Find each parasitized red blood cell.
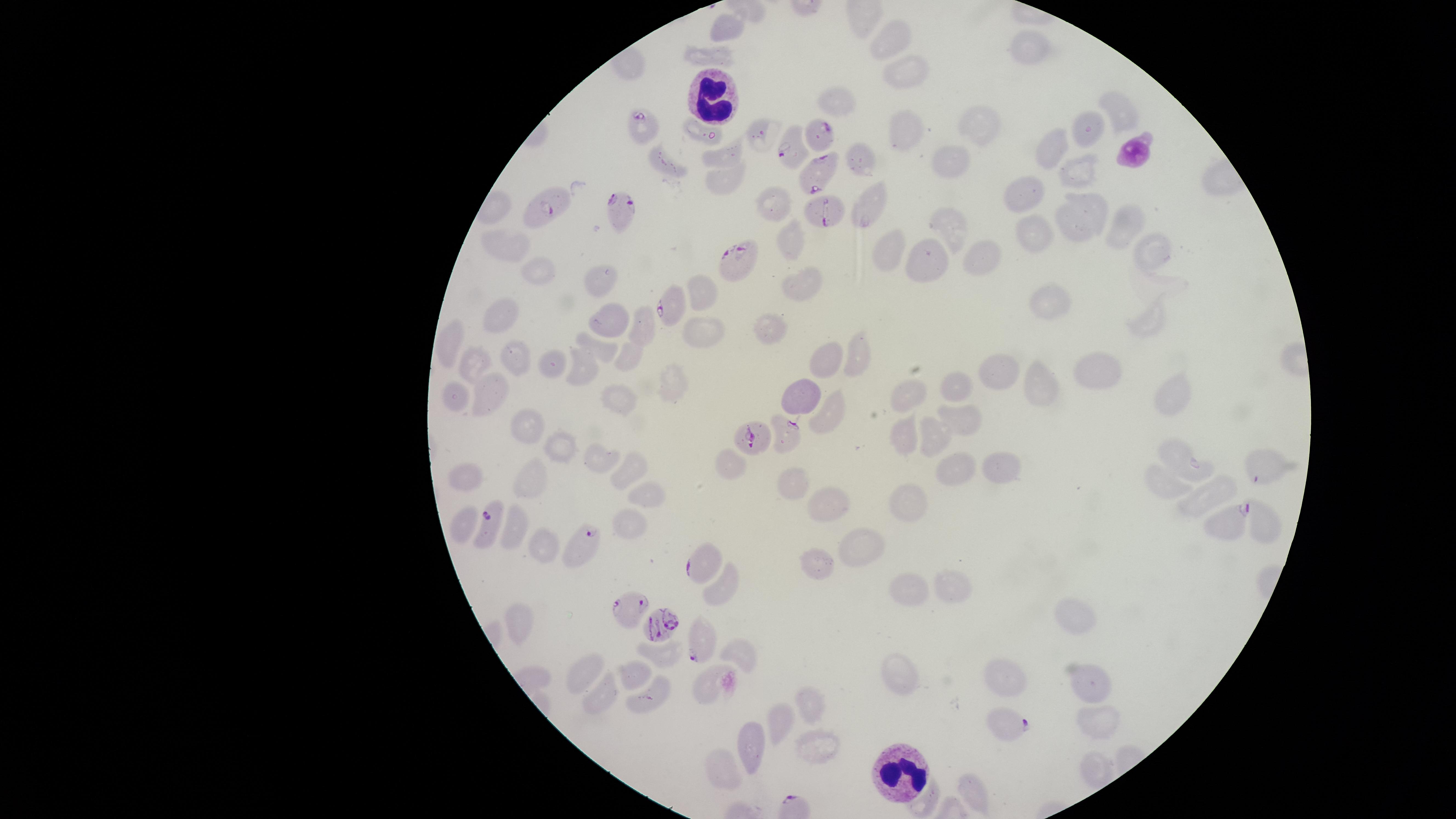
Approximate marker points as {x, y} in pixels.
Parasitized red blood cells: {644, 127}, {818, 140}, {790, 148}, {817, 173}, {547, 203}, {821, 208}, {623, 211}, {739, 260}, {672, 304}, {791, 431}, {754, 441}, {1229, 517}, {490, 525}, {583, 542}, {699, 561}, {627, 605}, {655, 626}, {701, 643}, {1005, 721}.

Approximate marker points as {x, y} in pixels. White blood cells: {711, 100}, {899, 770}. Uninfected red blood cells: {724, 26}, {890, 36}, {1026, 46}, {717, 54}, {905, 71}, {840, 103}, {1120, 119}, {984, 123}, {905, 130}, {701, 134}, {756, 135}, {1081, 136}, {1054, 144}, {858, 157}, {718, 159}, {951, 161}, {1073, 163}, {671, 167}, {727, 178}, {1022, 194}, {874, 202}, {775, 203}, {1083, 214}, {1123, 220}, {951, 226}, {1040, 235}, {1152, 245}, {790, 246}, {516, 248}, {891, 249}, {933, 256}, {983, 257}, {543, 270}, {601, 283}, {802, 286}, {700, 290}, {1056, 303}, {504, 316}, {1147, 318}, {606, 322}, {701, 325}, {776, 326}, {642, 328}, {451, 339}, {603, 349}, {854, 352}, {627, 356}, {827, 358}, {513, 360}, {583, 361}, {549, 363}, {478, 365}, {995, 366}, {1094, 369}, {1033, 376}, {674, 381}, {956, 384}, {1173, 386}, {802, 393}, {455, 395}, {493, 395}, {902, 397}, {619, 399}, {827, 406}, {964, 420}, {530, 423}, {929, 434}, {899, 436}, {564, 450}, {726, 459}, {1185, 459}, {606, 464}, {998, 466}, {951, 467}, {1260, 469}, {629, 471}, {468, 479}, {527, 482}, {795, 482}, {1167, 487}, {650, 495}, {1207, 499}, {912, 501}, {829, 507}, {462, 524}, {1263, 524}, {627, 525}, {512, 534}, {860, 543}, {542, 548}, {818, 566}, {913, 585}, {721, 588}, {951, 589}, {522, 620}, {1081, 625}, {740, 651}, {668, 657}, {586, 673}, {906, 676}, {634, 678}, {1017, 680}, {1093, 682}, {707, 683}, {652, 695}, {603, 696}, {806, 704}, {780, 718}, {1095, 718}, {815, 738}, {748, 744}, {725, 763}. Giemsa-stained preparation. Circular visible region. Single field of view. Species: Plasmodium falciparum. Thin smear of blood. Image is 1456×819 pixels. Smartphone photograph through the microscope eyepiece.